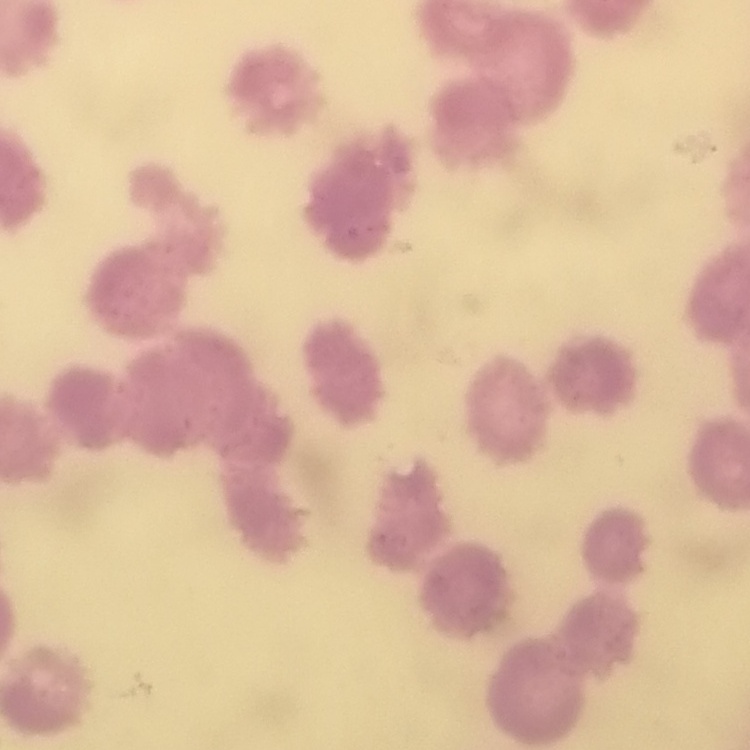 The erythrocytes exhibit rouleaux formation. Square crop of a larger photomicrograph. Stained with either Field's or Giemsa. Thin blood smear.